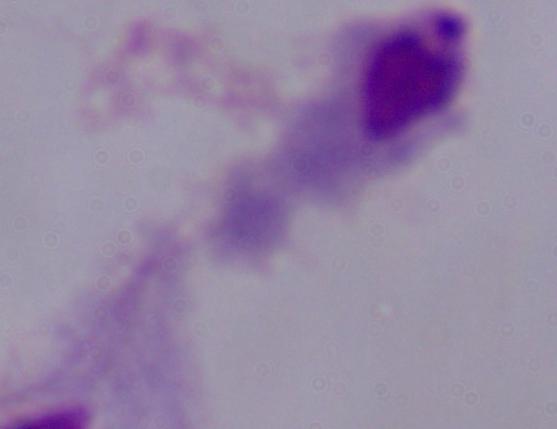
magnification = 1000x
identification = trichomonad
modality = photomicrograph